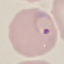

Result: malaria parasites identified. Cell patch, automatically extracted from a larger field of view and resized to 64 × 64 pixels. Thin blood smear. Acquired by smartphone through the microscope eyepiece. Giemsa-stained preparation.